Comment on the morphology of the erythrocytes.
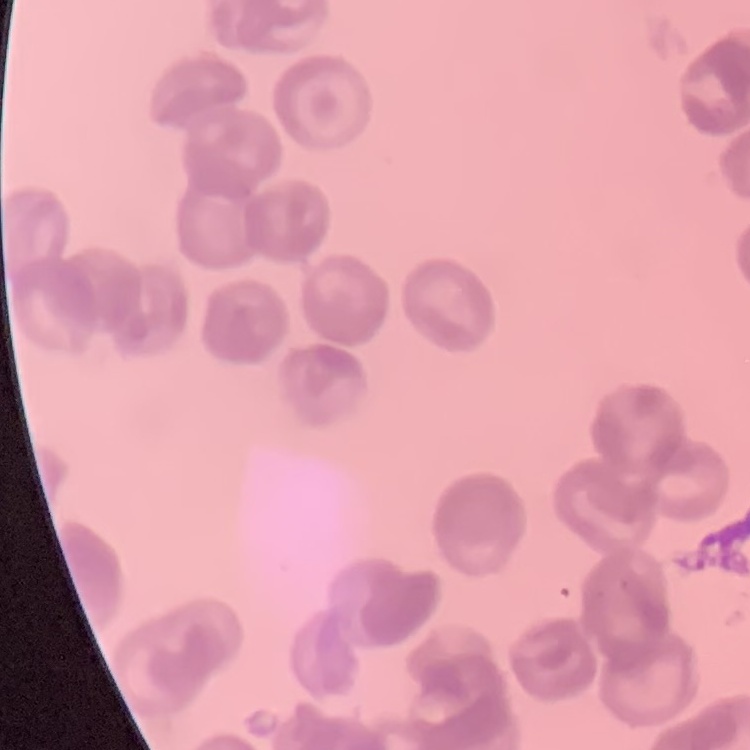
They show rouleaux formation.

One tile cut from a larger photomicrograph. Stained with either Field's or Giemsa. Thin blood film.